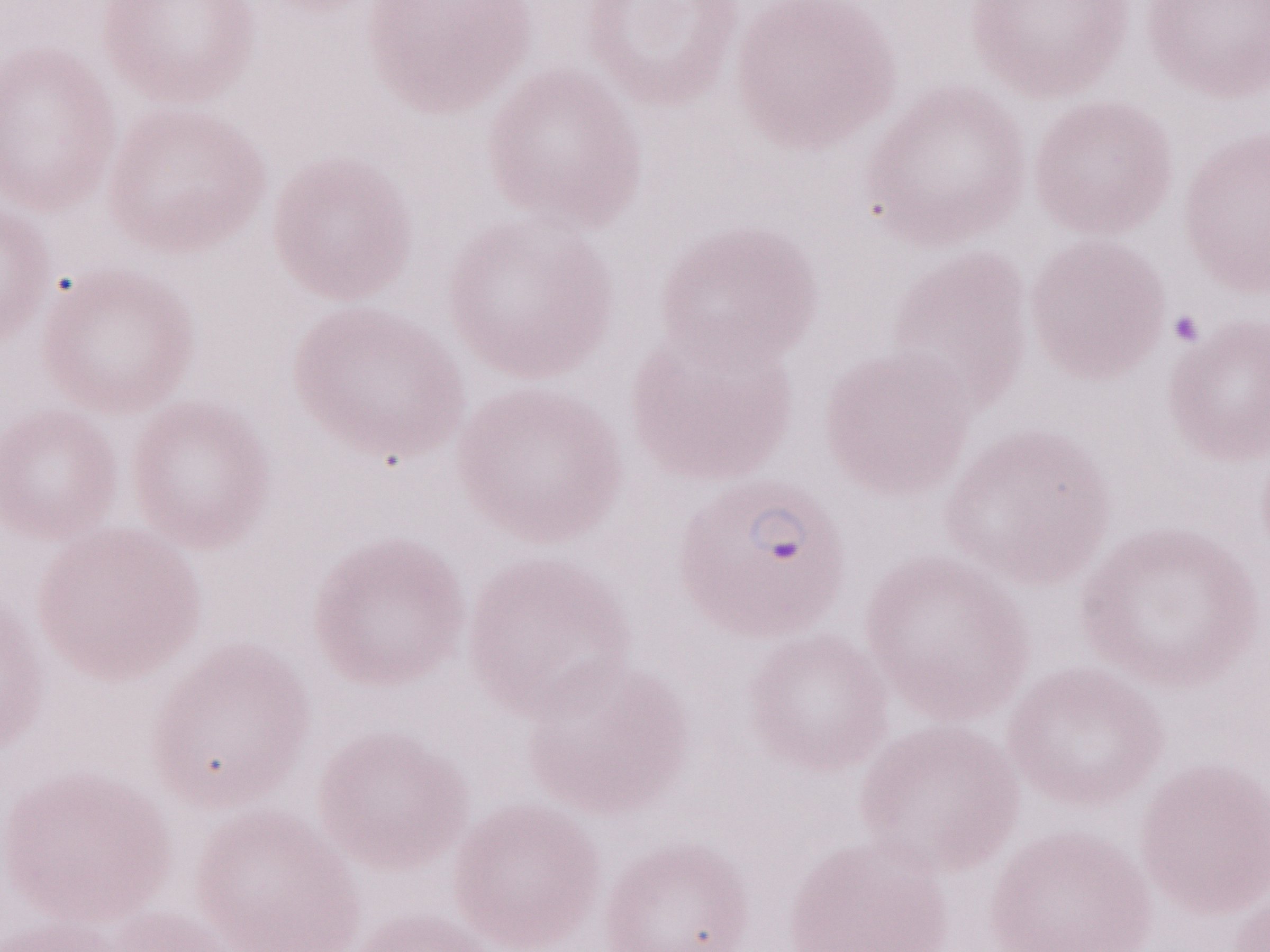 Thin blood film. 1,000x magnification. Patient diagnosis: malaria infection. May-Grünwald-Giemsa stain. Image is 1270×952 pixels. Single field of view. Olympus BX43 microscope and DP73 digital camera.